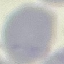
Summary:
  - Malaria status: uninfected
  - Image type: cell patch, automatically extracted from a larger field of view and resized to 64 × 64 pixels
  - Capture: smartphone through the microscope eyepiece
  - Preparation: thin smear
  - Stain: Giemsa